Outline platelets.
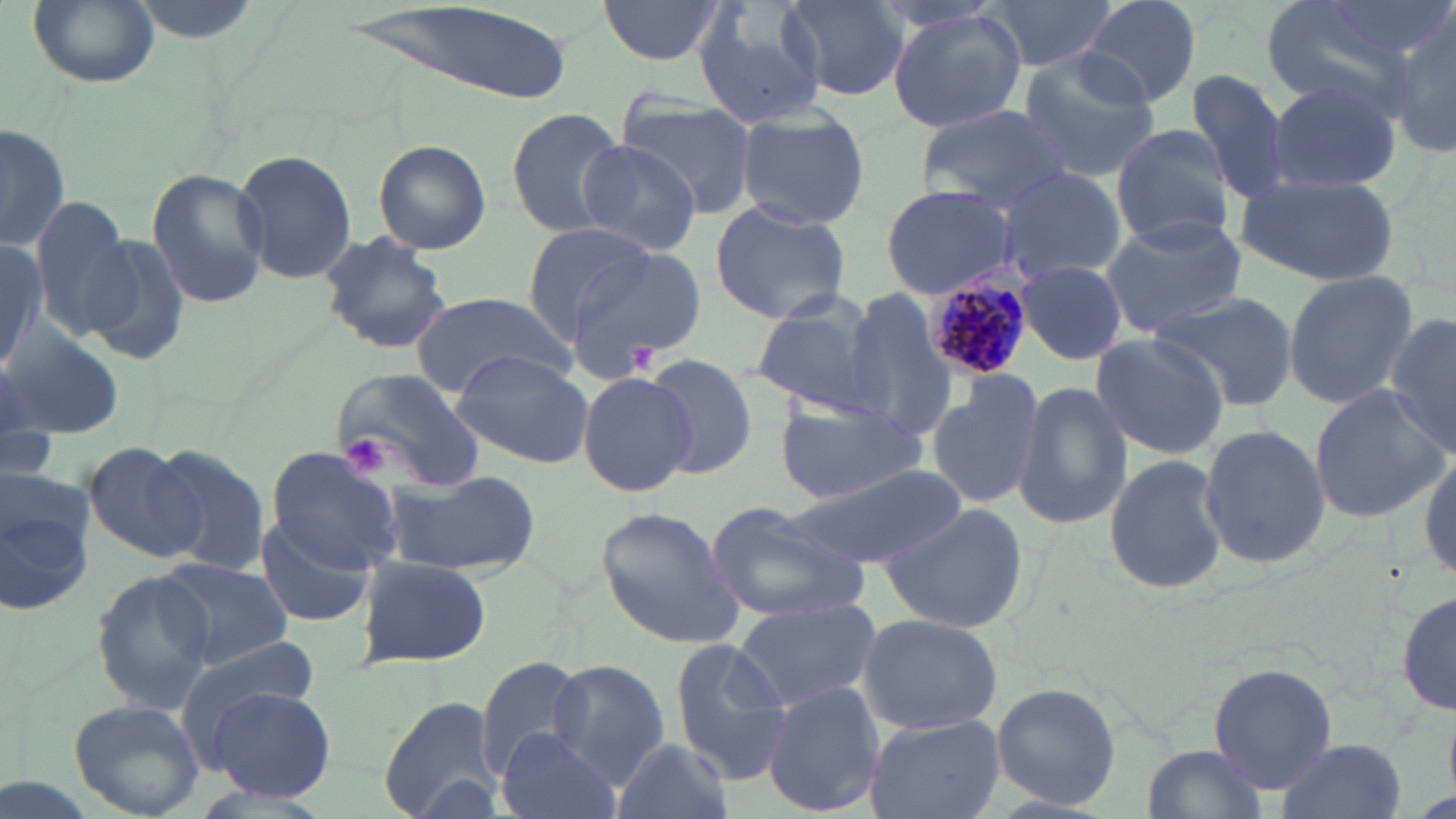

Approximate bounding boxes as (x1, y1, x2, y2) in pixels.
Platelets: (631, 342, 662, 374), (343, 434, 390, 475).

Plasmodium malariae-infected red blood cell locations = approximate bounding boxes as (x1, y1, x2, y2) in pixels: (923, 260, 1030, 378)
slide-level diagnosis = Plasmodium malariae
modality = light microscopy
preparation = thin blood smear
field of view = single
uninfected red blood cell locations = approximate bounding boxes as (x1, y1, x2, y2) in pixels: (26, 0, 162, 89), (597, 0, 726, 65), (776, 0, 912, 105), (983, 0, 1125, 71), (1078, 0, 1201, 108), (1261, 0, 1423, 117), (694, 2, 830, 127), (347, 5, 580, 106), (884, 7, 1028, 135), (1387, 11, 1456, 162), (1015, 47, 1163, 180), (1188, 66, 1295, 207), (1266, 76, 1402, 196), (618, 99, 759, 220), (915, 104, 1075, 208), (505, 107, 627, 239), (736, 110, 871, 230), (1, 121, 73, 250), (1111, 123, 1240, 249), (373, 139, 492, 254), (575, 140, 701, 254), (232, 149, 357, 285), (993, 167, 1128, 284), (146, 168, 270, 310), (1237, 172, 1400, 285), (880, 185, 1021, 298), (27, 197, 140, 338), (709, 201, 851, 324), (1098, 213, 1246, 337), (520, 222, 657, 343), (0, 228, 47, 375), (317, 230, 453, 355), (82, 233, 190, 369), (563, 247, 706, 376), (1015, 260, 1130, 366), (1282, 268, 1418, 407), (837, 290, 956, 439), (410, 291, 573, 400), (1150, 291, 1297, 411), (751, 294, 887, 417), (1386, 314, 1456, 456), (0, 325, 125, 441), (1089, 333, 1230, 460), (448, 351, 594, 468), (645, 353, 760, 478), (332, 368, 486, 495), (927, 370, 1047, 512), (578, 371, 697, 496), (1015, 382, 1132, 531), (1308, 383, 1449, 526), (774, 398, 926, 505), (1197, 421, 1329, 572), (83, 442, 204, 562), (146, 444, 272, 575), (265, 444, 405, 574), (1416, 451, 1455, 589), (1102, 452, 1228, 597), (0, 464, 97, 621), (789, 464, 968, 573), (382, 469, 538, 577), (880, 500, 1030, 633), (704, 501, 872, 623), (596, 507, 743, 651), (254, 511, 377, 629), (355, 553, 489, 670), (155, 556, 293, 669), (90, 568, 218, 710), (1396, 590, 1456, 718), (733, 595, 881, 712), (855, 612, 1002, 735), (670, 638, 794, 781), (175, 639, 321, 741), (474, 656, 592, 780), (546, 660, 669, 785), (1208, 660, 1337, 793), (763, 682, 883, 816), (989, 683, 1122, 811), (207, 686, 335, 803), (376, 692, 504, 819), (70, 699, 203, 818), (863, 714, 1005, 819), (494, 729, 623, 819), (612, 738, 734, 819), (1274, 738, 1405, 819), (1143, 744, 1272, 819)
image size = 1456×819 pixels
stain = May-Grünwald-Giemsa
magnification = 1000x